Describe the morphology of the red blood cells.
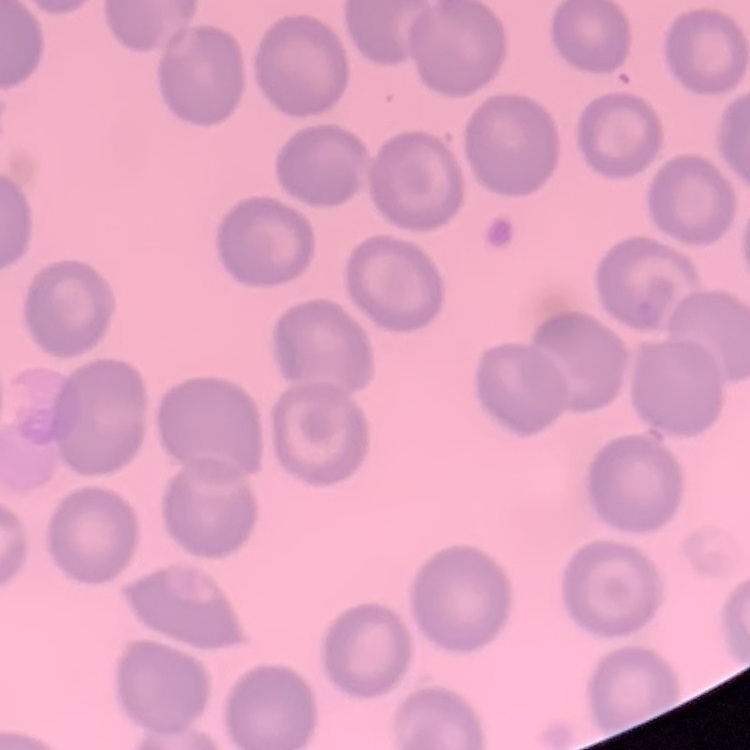

No rouleaux formation.

Square crop of a larger photomicrograph. Stained with either Field's or Giemsa. Thin blood smear.